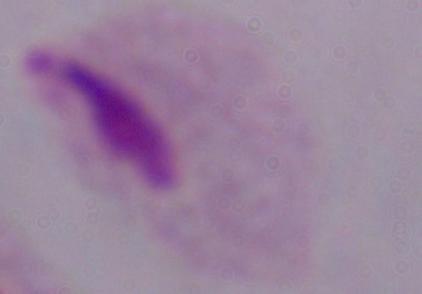

Summary:
  - Modality: micrograph
  - Identification: trichomonad
  - Magnification: 1000x